Assess for Plasmodium parasites.
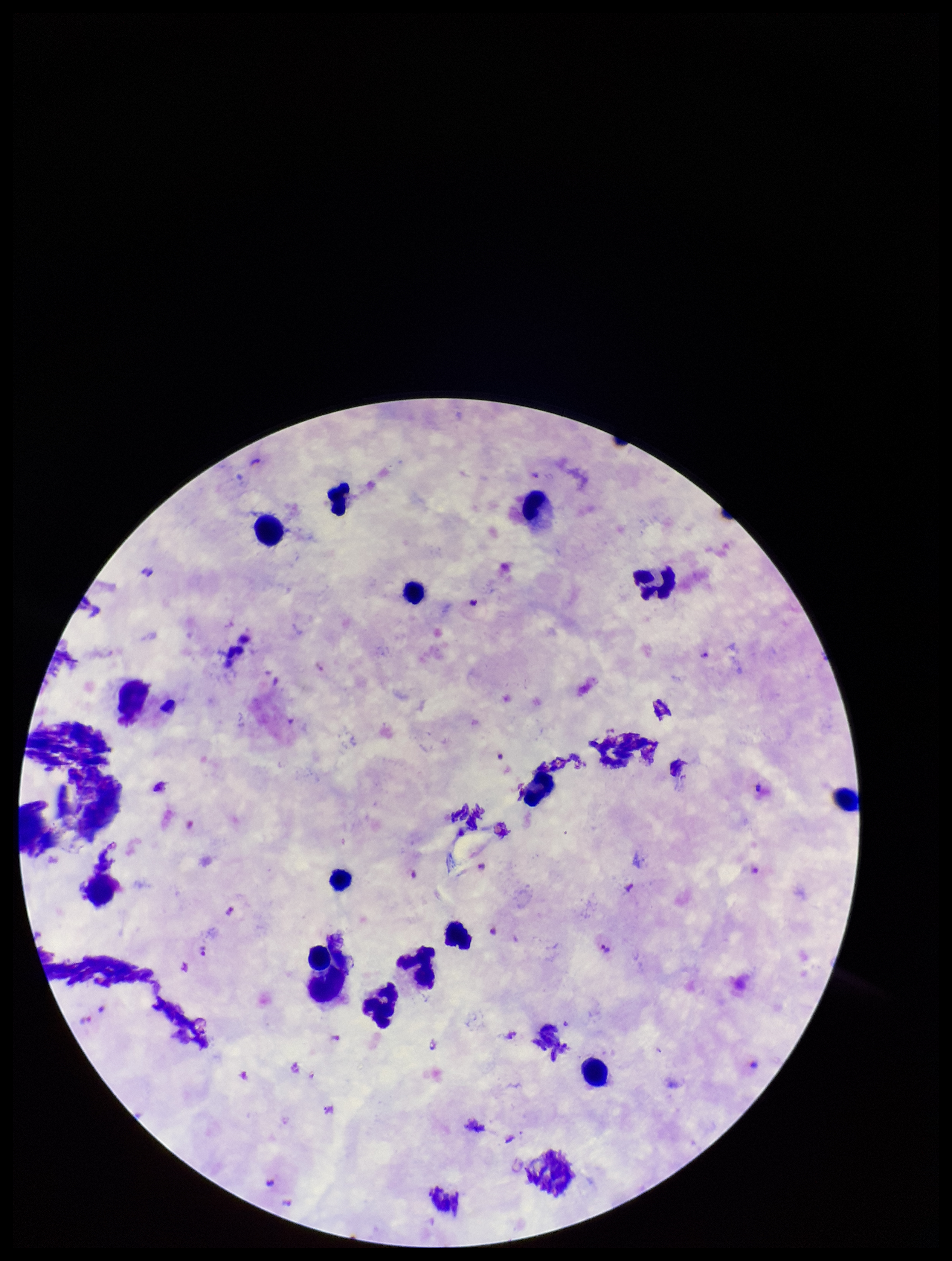
Detected.

image_size: 952×1261 pixels
capture: smartphone photograph through the microscope eyepiece
patient_malaria_status: positive
species_reported_for_this_patient: Plasmodium falciparum
stain: Giemsa
preparation: thick
leukocyte_count: 13
parasite_count: 11
field_of_view: single